Give the location of every white blood cell.
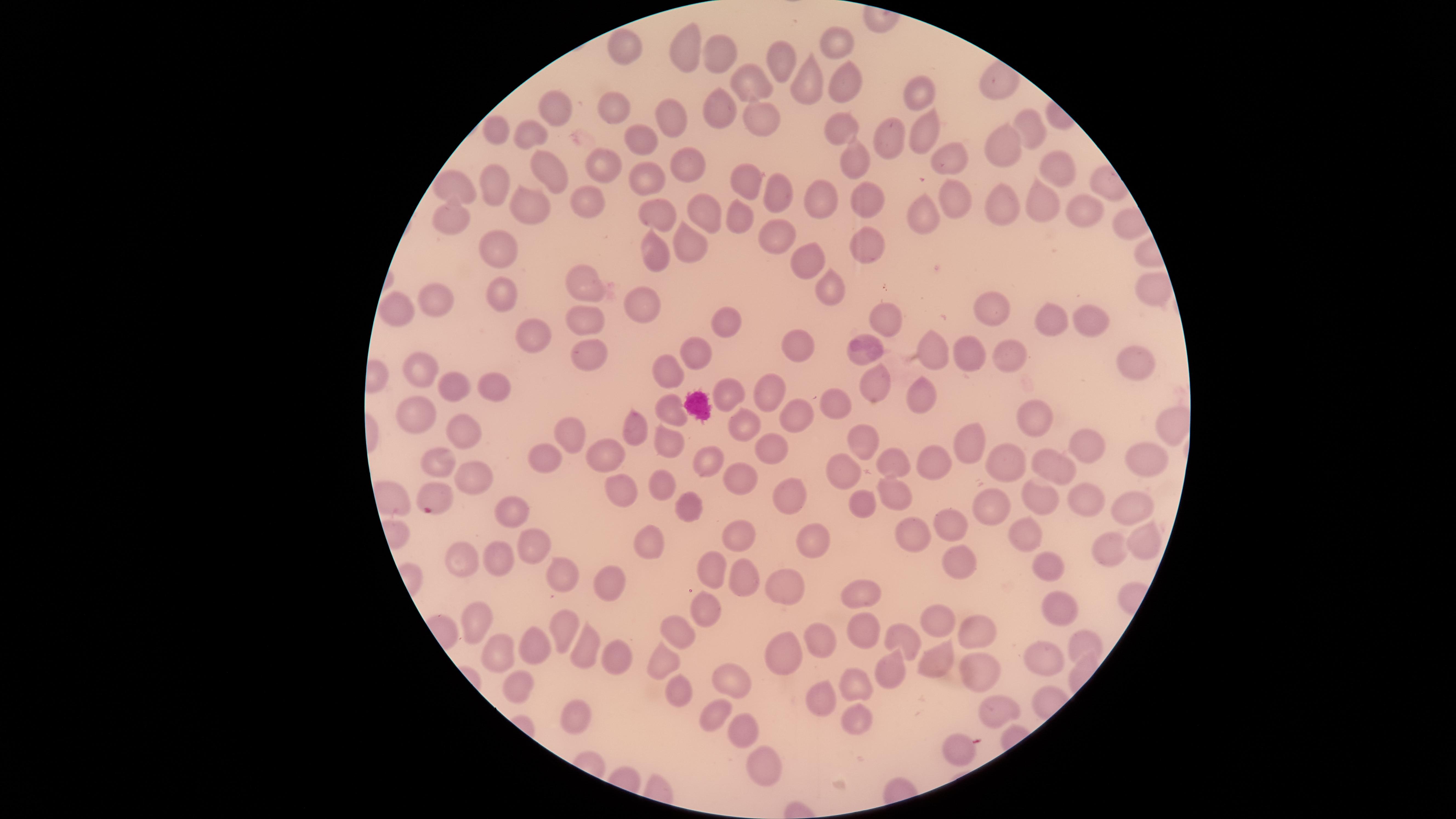

No white blood cells identified.

capture = smartphone photograph through the microscope eyepiece
preparation = thin blood film
field of view = single
presence = malaria parasites seen
parasitized red blood cells = approximate marker points, in pixels from the top-left corner: (x=431, y=501)
image size = 1456×819 pixels
visible region = circular
species = Plasmodium falciparum
stain = Giemsa
uninfected red blood cells = approximate marker points, in pixels from the top-left corner: (x=837, y=42), (x=626, y=49), (x=686, y=49), (x=722, y=52), (x=779, y=65), (x=845, y=83), (x=750, y=87), (x=806, y=89), (x=919, y=89), (x=554, y=108), (x=619, y=109), (x=717, y=111), (x=759, y=117), (x=676, y=123), (x=496, y=128), (x=1025, y=128), (x=843, y=130), (x=927, y=133), (x=530, y=135), (x=643, y=139), (x=888, y=141), (x=948, y=150), (x=1000, y=151), (x=1052, y=162), (x=687, y=163), (x=855, y=164), (x=601, y=171), (x=550, y=176), (x=645, y=176), (x=738, y=184), (x=492, y=186), (x=455, y=192), (x=1040, y=194), (x=774, y=196), (x=951, y=197), (x=822, y=202), (x=1004, y=203), (x=867, y=204), (x=586, y=205), (x=1085, y=208), (x=528, y=210), (x=657, y=213), (x=700, y=213), (x=921, y=217), (x=451, y=220), (x=738, y=225), (x=768, y=235), (x=866, y=243), (x=490, y=248), (x=685, y=252), (x=655, y=256), (x=803, y=264), (x=580, y=287), (x=832, y=288), (x=500, y=296), (x=435, y=303), (x=643, y=305), (x=999, y=305), (x=1085, y=317), (x=404, y=318), (x=726, y=322), (x=885, y=322), (x=1053, y=322), (x=525, y=324), (x=585, y=324), (x=932, y=345), (x=795, y=348), (x=966, y=353), (x=692, y=354), (x=868, y=355), (x=588, y=356), (x=1015, y=356), (x=1137, y=366), (x=416, y=369), (x=669, y=372), (x=488, y=383), (x=874, y=385), (x=457, y=387), (x=767, y=388), (x=726, y=394), (x=921, y=399), (x=666, y=407), (x=836, y=408), (x=791, y=411), (x=412, y=417), (x=1036, y=419), (x=1167, y=423), (x=741, y=424), (x=629, y=428), (x=459, y=430), (x=565, y=437), (x=968, y=441), (x=666, y=443), (x=866, y=443), (x=1092, y=443), (x=769, y=446), (x=607, y=453), (x=1144, y=454), (x=712, y=456), (x=546, y=459), (x=1009, y=460), (x=433, y=461), (x=899, y=464), (x=936, y=464), (x=1047, y=464), (x=475, y=473), (x=844, y=473), (x=735, y=477), (x=658, y=485), (x=614, y=488), (x=786, y=491), (x=893, y=493), (x=1090, y=499), (x=686, y=502), (x=984, y=502), (x=1034, y=502), (x=857, y=505), (x=1131, y=505), (x=512, y=517), (x=944, y=528), (x=736, y=537), (x=910, y=537), (x=1141, y=537), (x=811, y=538), (x=1025, y=538), (x=652, y=543), (x=529, y=546), (x=1110, y=553), (x=952, y=556), (x=465, y=561), (x=496, y=561), (x=717, y=564), (x=561, y=569), (x=1049, y=569), (x=743, y=579), (x=787, y=583), (x=610, y=585), (x=858, y=594), (x=708, y=605), (x=1053, y=605), (x=474, y=612), (x=561, y=620), (x=933, y=623), (x=973, y=628), (x=860, y=629), (x=678, y=634), (x=820, y=634), (x=904, y=639), (x=583, y=645), (x=1089, y=647), (x=537, y=648), (x=493, y=649), (x=787, y=653), (x=610, y=657), (x=936, y=662), (x=1043, y=662), (x=664, y=666), (x=974, y=668), (x=892, y=671), (x=734, y=679), (x=854, y=682), (x=517, y=687), (x=674, y=694), (x=821, y=696), (x=1002, y=708), (x=578, y=714), (x=713, y=715), (x=853, y=723), (x=738, y=725), (x=956, y=751), (x=759, y=764)